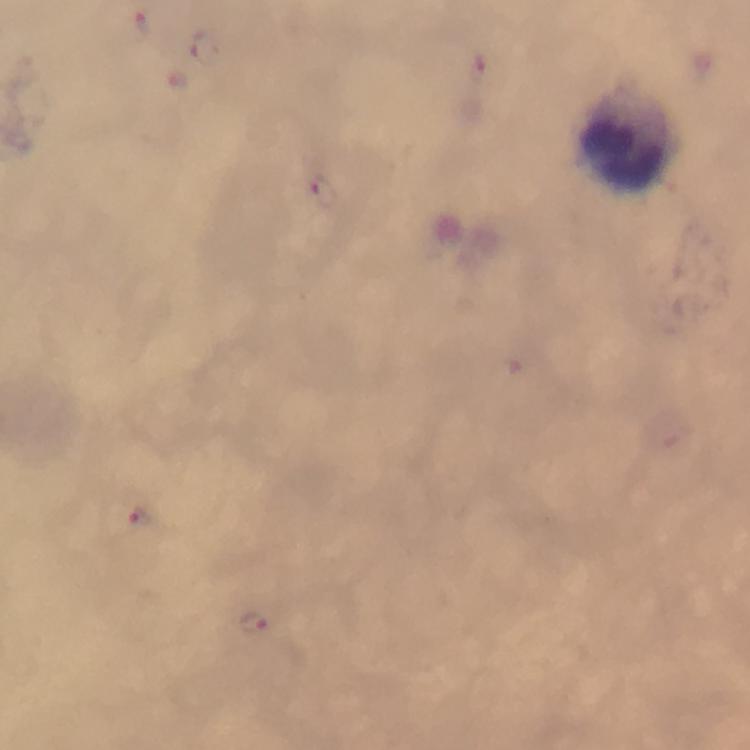
Approximate centers as (x, y) in pixels.
Summary:
  - Malaria parasite locations: (139, 28), (209, 48), (322, 191), (140, 517), (252, 622)
  - Leukocyte locations: (628, 139)
  - Capture: smartphone camera through the microscope
  - Immersion oil: applied
  - Image size: 750×750 pixels
  - Cropped from: a single field of view
  - Context: from a diagnostic examination for malaria
  - Magnification: 100x
  - Stain: Giemsa
  - Preparation: thick blood film